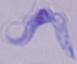
Summary:
  - Identification: trypanosome
  - Modality: micrograph
  - Magnification: 1000x